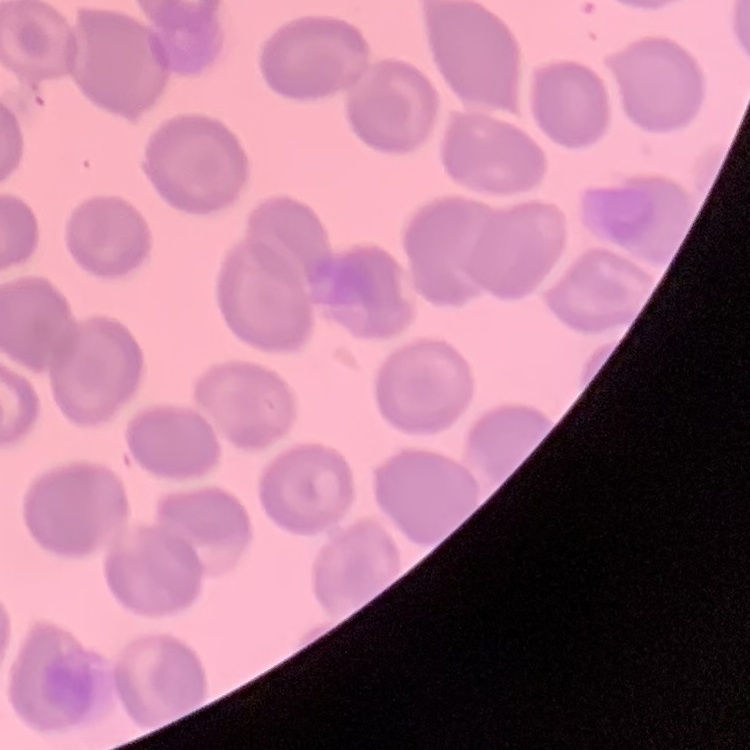
The erythrocytes show no rouleaux formation. Field's or Giemsa stain. Thin peripheral smear. One tile cut from a larger photomicrograph.